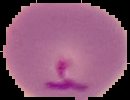

Summary:
  - Malaria status: parasitized
  - Image size: 130×100 pixels
  - Preparation: thin blood smear
  - Image type: segmented cell region with the area outside set to black